Classify this cell by malaria status.
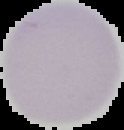
Uninfected.

From a thin blood smear. Cell region segmented out of the field of view; the surrounding area is masked to black. Image is 124×130 pixels.